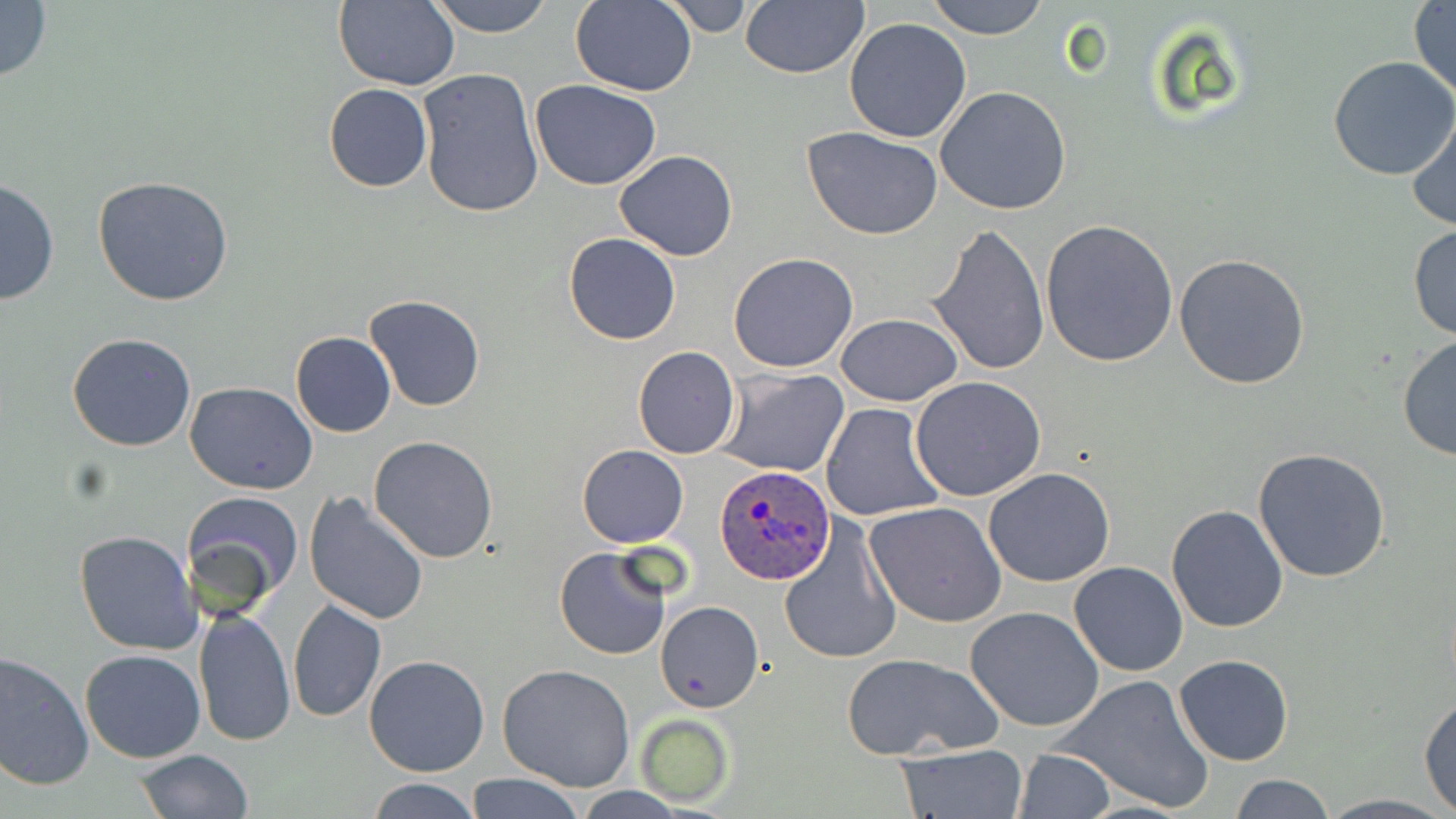
{
  "slide_level_diagnosis": "Plasmodium ovale",
  "uninfected_red_blood_cell_locations": "approximate bounding boxes as (x1, y1, x2, y2) in pixels: (0, 0, 52, 85), (425, 0, 556, 38), (659, 0, 759, 38), (925, 0, 1051, 41), (333, 1, 460, 92), (571, 1, 696, 96), (739, 1, 869, 78), (1408, 1, 1455, 100), (845, 16, 972, 142), (1328, 55, 1456, 180), (417, 67, 545, 217), (530, 81, 661, 189), (323, 83, 433, 192), (935, 85, 1074, 215), (1407, 111, 1456, 233), (802, 127, 946, 240), (614, 149, 738, 261), (0, 175, 60, 308), (93, 175, 235, 307), (1041, 219, 1179, 366), (928, 223, 1049, 377), (1407, 224, 1456, 342), (564, 232, 680, 345), (728, 253, 859, 373), (1173, 254, 1312, 391), (365, 295, 485, 412), (835, 312, 961, 407), (65, 332, 197, 452), (290, 332, 396, 437), (1396, 335, 1455, 462), (632, 347, 741, 460), (718, 367, 850, 476), (910, 376, 1046, 503), (185, 382, 317, 495), (822, 402, 945, 520), (369, 436, 498, 562), (577, 445, 689, 547), (1252, 446, 1394, 582), (983, 467, 1116, 587), (182, 489, 305, 610), (303, 492, 430, 626), (865, 501, 1007, 627), (1166, 505, 1289, 631), (779, 522, 900, 665), (73, 529, 200, 656), (555, 547, 672, 661), (1067, 561, 1188, 677), (288, 599, 385, 721), (657, 602, 763, 713), (965, 605, 1104, 732), (194, 607, 295, 745), (79, 648, 206, 763), (0, 650, 95, 792), (839, 651, 1003, 759), (364, 654, 490, 775), (1173, 654, 1293, 766), (498, 665, 637, 792), (1055, 673, 1216, 814), (1419, 692, 1456, 813), (634, 713, 736, 808), (895, 743, 1028, 818), (135, 748, 252, 819), (1012, 748, 1117, 818), (464, 772, 588, 819), (1229, 774, 1339, 818), (365, 778, 483, 818), (1315, 793, 1454, 818)",
  "plasmodium_ovale_infected_red_blood_cell_locations": "approximate bounding boxes as (x1, y1, x2, y2) in pixels: (714, 466, 834, 585)",
  "magnification": "1000x",
  "stain": "May-Grünwald-Giemsa",
  "preparation": "thin blood smear",
  "field_of_view": "one of a larger specimen",
  "image_size": "1456×819 pixels",
  "modality": "optical microscopy"
}